State which parasite is depicted.
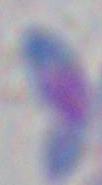

This is Toxoplasma gondii.

Summary:
  - Magnification: 1000x
  - Modality: photomicrograph